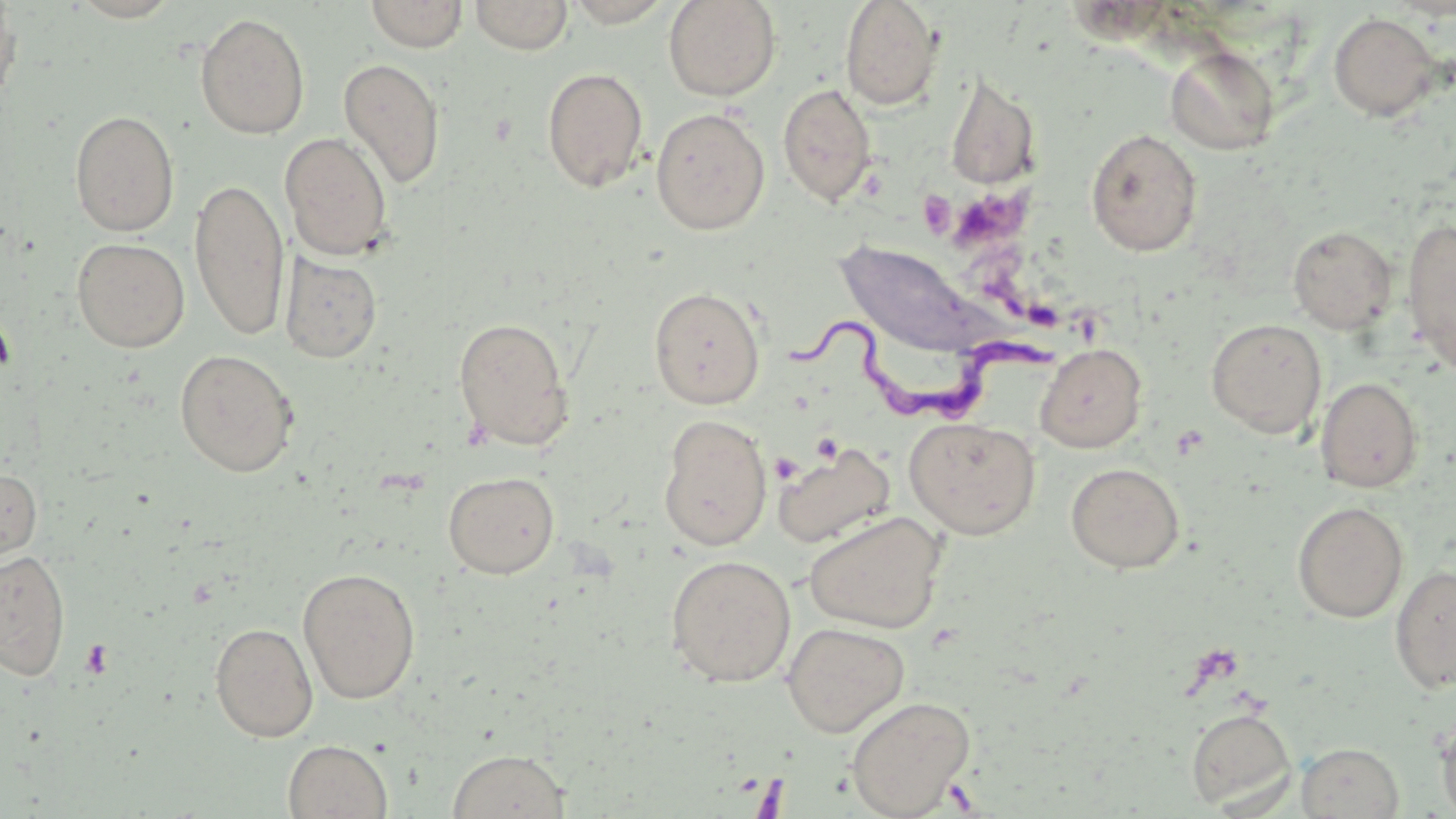
Summary:
  - Coordinate format: approximate bounding boxes as [x1, y1, x2, y2] in pixels
  - Uninfected red blood cell locations: [365, 0, 468, 51], [470, 0, 572, 55], [561, 0, 678, 27], [663, 0, 781, 101], [840, 0, 943, 111], [0, 3, 22, 111], [194, 12, 310, 139], [1328, 12, 1442, 121], [1165, 46, 1280, 155], [337, 57, 446, 189], [542, 67, 648, 193], [945, 74, 1041, 191], [777, 83, 877, 207], [650, 107, 770, 235], [69, 110, 180, 236], [1085, 128, 1203, 257], [280, 132, 393, 261], [189, 177, 290, 341], [1401, 218, 1456, 376], [1287, 225, 1398, 334], [72, 237, 190, 352], [834, 239, 997, 357], [280, 252, 382, 364], [649, 286, 765, 409], [453, 316, 575, 452], [1206, 318, 1327, 438], [1034, 343, 1147, 453], [174, 349, 299, 477], [1315, 377, 1423, 492], [658, 414, 772, 551], [904, 416, 1041, 540], [772, 442, 896, 549], [1065, 462, 1185, 573], [0, 467, 42, 568], [443, 471, 559, 578], [1292, 501, 1409, 623], [804, 511, 947, 633], [0, 548, 71, 680], [665, 554, 797, 687], [1390, 565, 1456, 693], [297, 567, 421, 704], [210, 622, 318, 742], [781, 622, 909, 737], [845, 696, 975, 817], [1186, 707, 1297, 812], [1436, 710, 1456, 818], [283, 739, 393, 819], [1297, 742, 1404, 818], [446, 748, 572, 818]
  - Trypanosoma brucei locations: [788, 302, 1071, 431]
  - Platelet locations: [956, 192, 1032, 258], [0, 313, 16, 379], [770, 453, 802, 484], [79, 639, 113, 679]
  - Slide-level diagnosis: Trypanosoma brucei
  - Image size: 1456×819 pixels
  - Stain: May-Grünwald-Giemsa
  - Magnification: 1000x
  - Preparation: thin blood smear
  - Field of view: one of a larger specimen
  - Modality: light microscopy